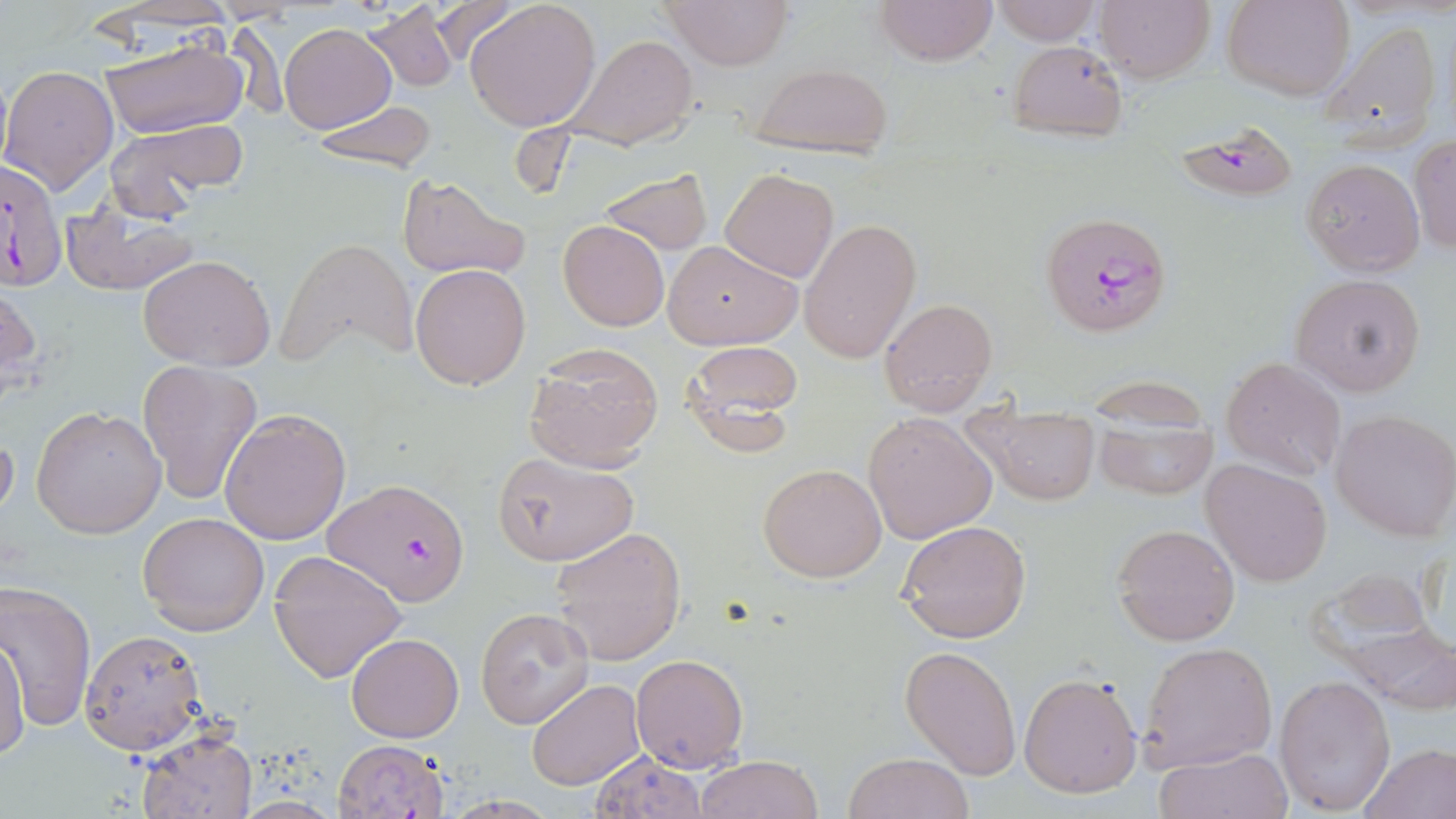

Summary:
  - Coordinate format: approximate bounding boxes as [x1, y1, x2, y2] in pixels
  - Plasmodium falciparum-infected red blood cell locations: [1172, 121, 1301, 205], [0, 159, 69, 292], [1046, 219, 1165, 333], [325, 478, 472, 606]
  - Uninfected red blood cell locations: [431, 0, 519, 67], [659, 0, 795, 69], [873, 0, 997, 67], [1096, 0, 1215, 84], [1224, 0, 1353, 101], [361, 1, 459, 93], [464, 1, 603, 132], [987, 1, 1103, 46], [90, 2, 243, 35], [1316, 19, 1446, 149], [281, 24, 394, 133], [559, 33, 700, 152], [101, 35, 248, 141], [1007, 40, 1128, 141], [746, 63, 896, 159], [1, 64, 118, 193], [306, 100, 438, 175], [104, 119, 248, 214], [1409, 138, 1456, 256], [1301, 158, 1425, 276], [597, 168, 713, 256], [720, 169, 839, 282], [395, 174, 530, 282], [62, 199, 201, 297], [799, 218, 922, 365], [558, 220, 670, 331], [280, 237, 419, 369], [662, 239, 802, 349], [138, 253, 276, 371], [410, 263, 531, 390], [1290, 273, 1426, 397], [1, 279, 41, 409], [879, 296, 998, 417], [676, 340, 805, 456], [522, 344, 664, 473], [1221, 356, 1346, 482], [136, 359, 263, 503], [31, 405, 167, 539], [219, 408, 350, 545], [961, 408, 1102, 507], [1091, 409, 1219, 501], [1330, 409, 1456, 541], [864, 412, 996, 543], [0, 428, 20, 526], [490, 451, 638, 566], [1200, 458, 1334, 586], [757, 462, 887, 583], [138, 512, 270, 636], [898, 519, 1032, 643], [1112, 524, 1239, 646], [550, 526, 687, 667], [267, 549, 407, 683], [1306, 568, 1441, 671], [1, 581, 99, 731], [476, 608, 594, 728], [1345, 624, 1456, 714], [79, 628, 207, 755], [346, 632, 464, 742], [1, 634, 29, 762], [1138, 641, 1278, 772], [900, 644, 1021, 780], [629, 653, 749, 773], [1019, 672, 1143, 797], [1275, 674, 1395, 813], [525, 679, 646, 790], [137, 728, 258, 819], [333, 737, 450, 818], [1358, 743, 1456, 818], [1155, 746, 1292, 819], [588, 751, 709, 817], [843, 753, 973, 819], [695, 755, 826, 818]
  - Slide-level diagnosis: Plasmodium falciparum
  - Field of view: one of a larger specimen
  - Image size: 1456×819 pixels
  - Modality: light microscopy
  - Preparation: thin blood film
  - Magnification: 1000x
  - Stain: May-Grünwald-Giemsa